Classify this cell by malaria status.
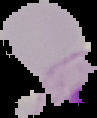
It is uninfected.

{
  "image_type": "segmented cell region on a black background",
  "image_size": "97×118 pixels",
  "preparation": "thin blood smear"
}